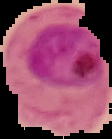 Malaria status: parasitized. From a thin blood film. Image is 112×139 pixels. The area outside the segmented cell region is set to black.